Assess the morphology of the erythrocytes.
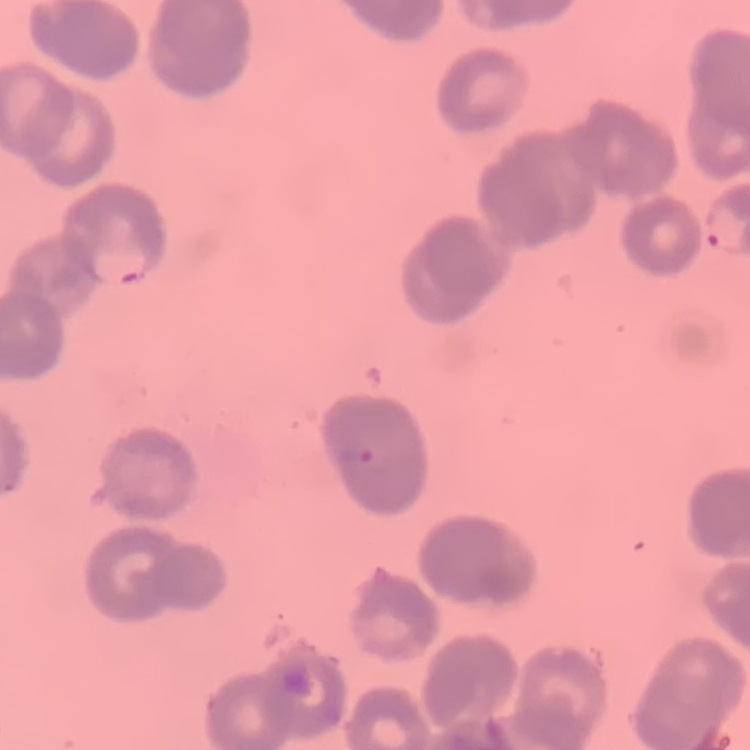
Rouleaux formation.

Field's or Giemsa stain. Square crop of a larger photomicrograph. Thin blood film.